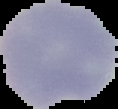

{
  "image_size": "118×109 pixels",
  "image_type": "segmented cell region on a black background",
  "preparation": "thin blood film",
  "result": "negative for Plasmodium parasites"
}